Report the malaria status of this cell.
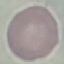
It is uninfected.

Giemsa stain. Acquired by smartphone through the microscope eyepiece. Automatically extracted cell patch, resized to 64 × 64 pixels. Thin blood film.